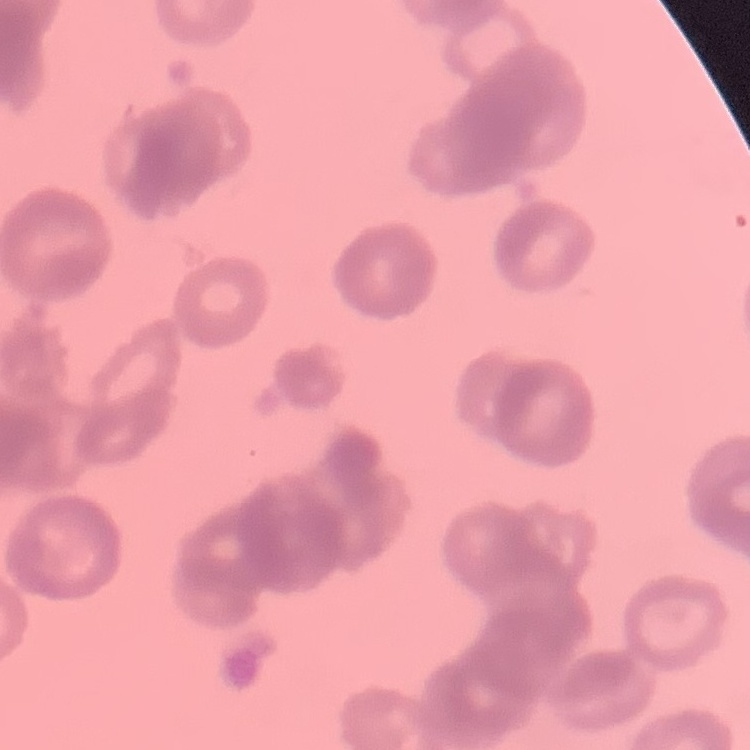

Summary:
  - Erythrocyte morphology: rouleaux formation
  - Preparation: thin blood film
  - Stain: Field's or Giemsa
  - Image type: one tile cut from a larger photomicrograph